Comment on the morphology of the red blood cells.
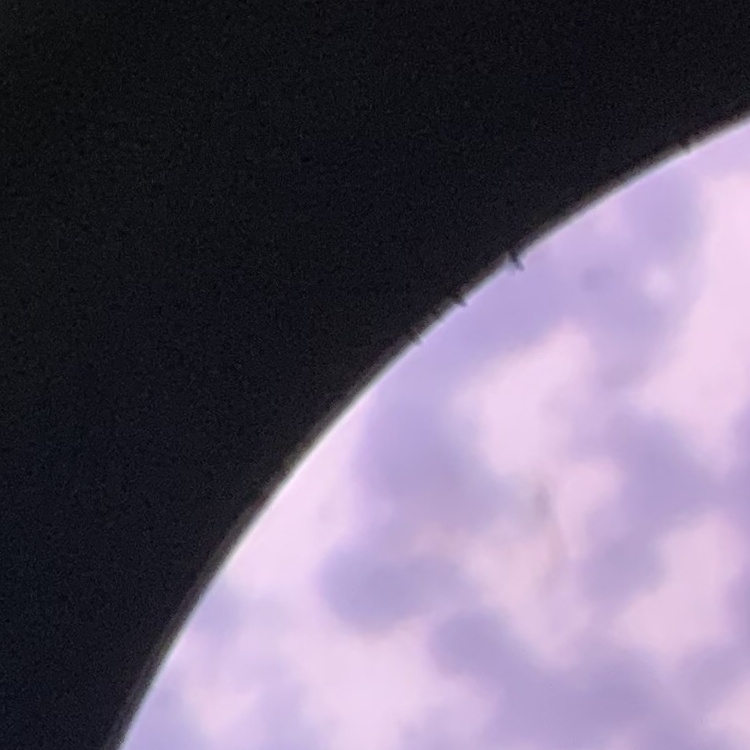
They show rouleaux formation.

Summary:
  - Preparation: thin blood film
  - Image type: square crop of a larger photomicrograph
  - Stain: Field's or Giemsa